Name the blood parasite species.
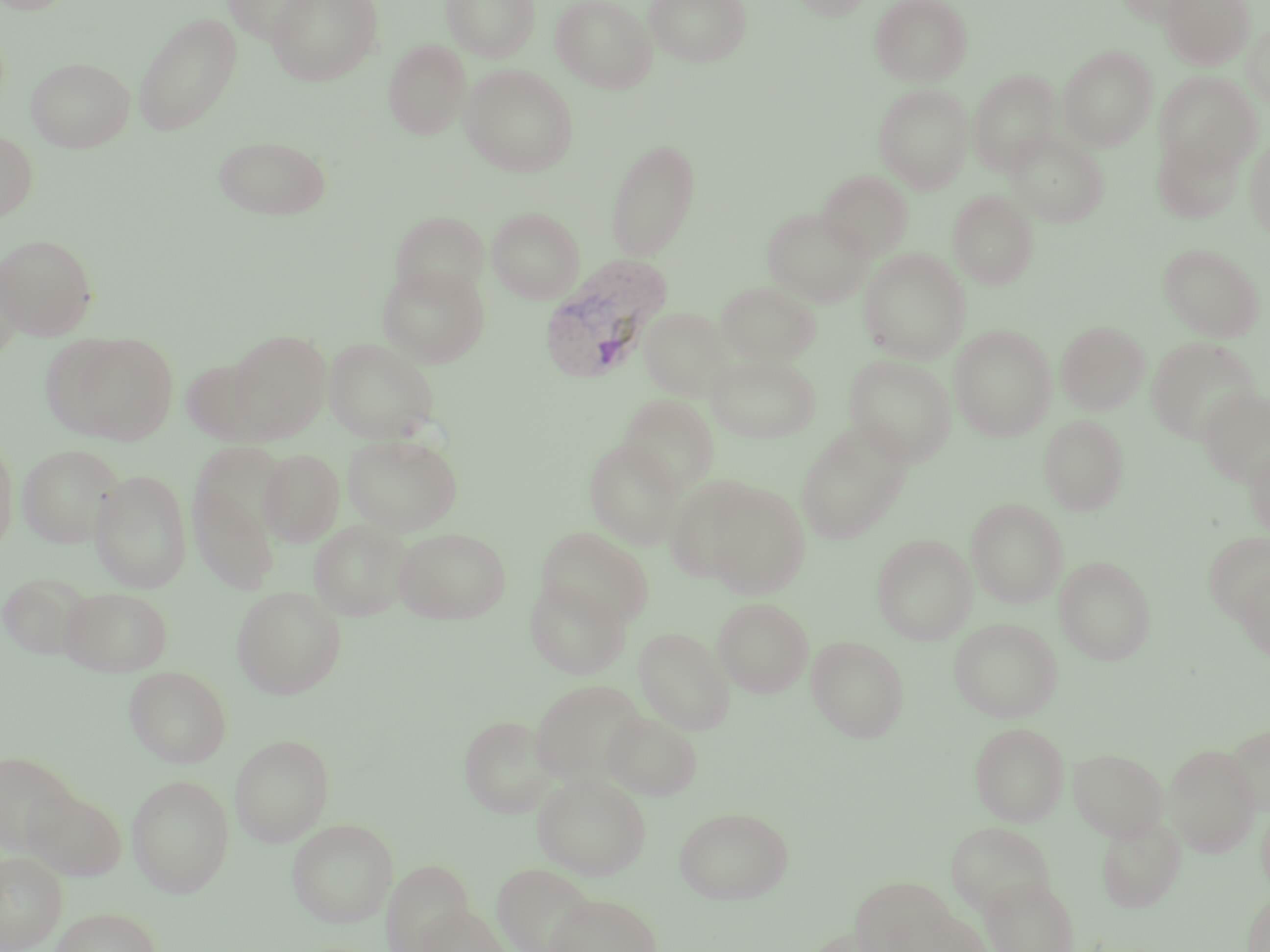

Plasmodium vivax.

Approximate bounding boxes as named x1/y1/x2/y2 corners in pixels. Plasmodium vivax-infected red blood cell locations: (x1=539, y1=257, x2=671, y2=385). Uninfected red blood cell locations: (x1=222, y1=0, x2=323, y2=44), (x1=267, y1=0, x2=383, y2=85), (x1=442, y1=0, x2=540, y2=61), (x1=552, y1=0, x2=656, y2=92), (x1=644, y1=0, x2=751, y2=66), (x1=792, y1=0, x2=873, y2=20), (x1=870, y1=0, x2=972, y2=85), (x1=1114, y1=0, x2=1210, y2=26), (x1=1159, y1=0, x2=1255, y2=70), (x1=133, y1=12, x2=243, y2=136), (x1=1242, y1=22, x2=1270, y2=109), (x1=384, y1=39, x2=471, y2=140), (x1=1058, y1=46, x2=1157, y2=150), (x1=26, y1=56, x2=135, y2=152), (x1=460, y1=64, x2=579, y2=176), (x1=969, y1=65, x2=1157, y2=163), (x1=968, y1=70, x2=1060, y2=174), (x1=1154, y1=72, x2=1261, y2=176), (x1=874, y1=83, x2=973, y2=193), (x1=0, y1=129, x2=38, y2=222), (x1=1006, y1=129, x2=1108, y2=227), (x1=1153, y1=133, x2=1245, y2=223), (x1=213, y1=134, x2=332, y2=219), (x1=1245, y1=137, x2=1270, y2=239), (x1=606, y1=139, x2=701, y2=261), (x1=818, y1=170, x2=912, y2=259), (x1=948, y1=190, x2=1038, y2=289), (x1=488, y1=207, x2=584, y2=303), (x1=763, y1=207, x2=872, y2=306), (x1=390, y1=212, x2=489, y2=302), (x1=0, y1=233, x2=98, y2=339), (x1=1159, y1=244, x2=1264, y2=341), (x1=859, y1=248, x2=970, y2=363), (x1=0, y1=250, x2=25, y2=364), (x1=377, y1=263, x2=489, y2=367), (x1=717, y1=282, x2=819, y2=365), (x1=638, y1=307, x2=734, y2=400), (x1=1056, y1=321, x2=1149, y2=414), (x1=1050, y1=322, x2=1138, y2=515), (x1=949, y1=324, x2=1056, y2=440), (x1=227, y1=329, x2=331, y2=441), (x1=46, y1=330, x2=179, y2=445), (x1=1146, y1=337, x2=1259, y2=443), (x1=324, y1=339, x2=440, y2=443), (x1=707, y1=352, x2=821, y2=442), (x1=845, y1=355, x2=956, y2=465), (x1=182, y1=358, x2=274, y2=445), (x1=1198, y1=387, x2=1270, y2=486), (x1=618, y1=395, x2=719, y2=494), (x1=1039, y1=414, x2=1128, y2=515), (x1=795, y1=424, x2=910, y2=544), (x1=0, y1=433, x2=19, y2=557), (x1=342, y1=433, x2=462, y2=535), (x1=584, y1=439, x2=684, y2=548), (x1=1245, y1=441, x2=1270, y2=540), (x1=190, y1=442, x2=293, y2=552), (x1=17, y1=444, x2=124, y2=548), (x1=258, y1=449, x2=345, y2=546), (x1=90, y1=469, x2=192, y2=593), (x1=663, y1=476, x2=761, y2=585), (x1=189, y1=478, x2=279, y2=594), (x1=701, y1=480, x2=810, y2=597), (x1=966, y1=498, x2=1067, y2=607), (x1=309, y1=519, x2=412, y2=621), (x1=393, y1=527, x2=511, y2=623), (x1=536, y1=527, x2=654, y2=627), (x1=1203, y1=533, x2=1270, y2=624), (x1=871, y1=534, x2=977, y2=644), (x1=1055, y1=556, x2=1156, y2=665), (x1=1236, y1=565, x2=1270, y2=660), (x1=1, y1=572, x2=93, y2=660), (x1=525, y1=578, x2=630, y2=679), (x1=61, y1=586, x2=173, y2=676), (x1=231, y1=586, x2=346, y2=699), (x1=712, y1=597, x2=813, y2=697), (x1=949, y1=617, x2=1062, y2=722), (x1=634, y1=628, x2=734, y2=734), (x1=807, y1=636, x2=909, y2=742), (x1=125, y1=665, x2=231, y2=767), (x1=530, y1=679, x2=648, y2=786), (x1=603, y1=711, x2=702, y2=800), (x1=459, y1=714, x2=555, y2=818), (x1=971, y1=722, x2=1068, y2=826), (x1=1222, y1=722, x2=1269, y2=815), (x1=230, y1=734, x2=334, y2=845), (x1=1164, y1=743, x2=1261, y2=857), (x1=1068, y1=747, x2=1168, y2=840), (x1=0, y1=750, x2=79, y2=853), (x1=533, y1=773, x2=651, y2=879), (x1=126, y1=775, x2=235, y2=898), (x1=23, y1=788, x2=127, y2=881), (x1=1257, y1=798, x2=1270, y2=900), (x1=674, y1=805, x2=794, y2=904), (x1=1096, y1=816, x2=1186, y2=912), (x1=287, y1=819, x2=398, y2=927), (x1=946, y1=820, x2=1054, y2=916), (x1=0, y1=851, x2=67, y2=952), (x1=383, y1=859, x2=473, y2=951), (x1=492, y1=862, x2=597, y2=952), (x1=981, y1=876, x2=1079, y2=952), (x1=852, y1=880, x2=962, y2=950), (x1=1242, y1=889, x2=1270, y2=952), (x1=543, y1=893, x2=663, y2=952), (x1=414, y1=903, x2=510, y2=952), (x1=882, y1=904, x2=991, y2=952), (x1=51, y1=907, x2=161, y2=952). Image is 1270×952 pixels. Light microscopy. One field of a larger specimen. Thin blood smear. Captured at 1000x magnification. May-Grünwald-Giemsa-stained preparation.